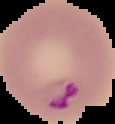

preparation: thin blood smear
image_size: 115×124 pixels
malaria_status: parasitized
image_type: segmented cell region on a black background